Classify this cell by malaria status.
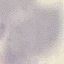

It is uninfected.

stain = Giemsa
image type = automatically extracted cell patch, resized to 64 × 64 pixels
capture = smartphone camera at the microscope eyepiece
preparation = thin smear